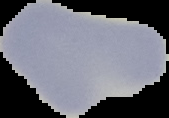
image type = segmented cell region on a black background
image size = 169×118 pixels
malaria status = uninfected
preparation = thin blood film